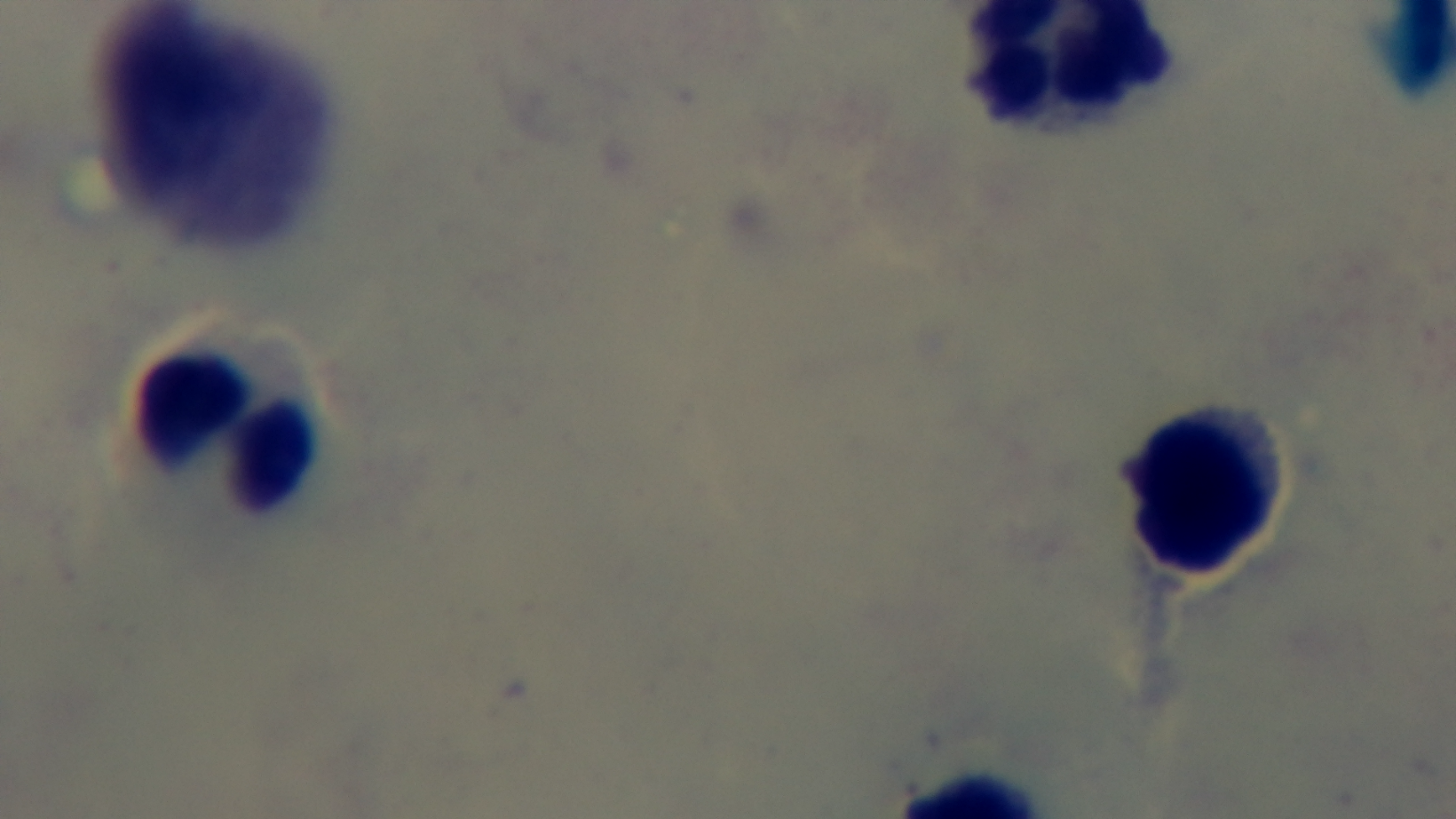
One field from the slide. Captured with a mounted 4K digital camera. Malaria status: uninfected. Giemsa stain. Preparation: thick. 100x oil-immersion objective. Photomicrograph.